Give the preparation type.
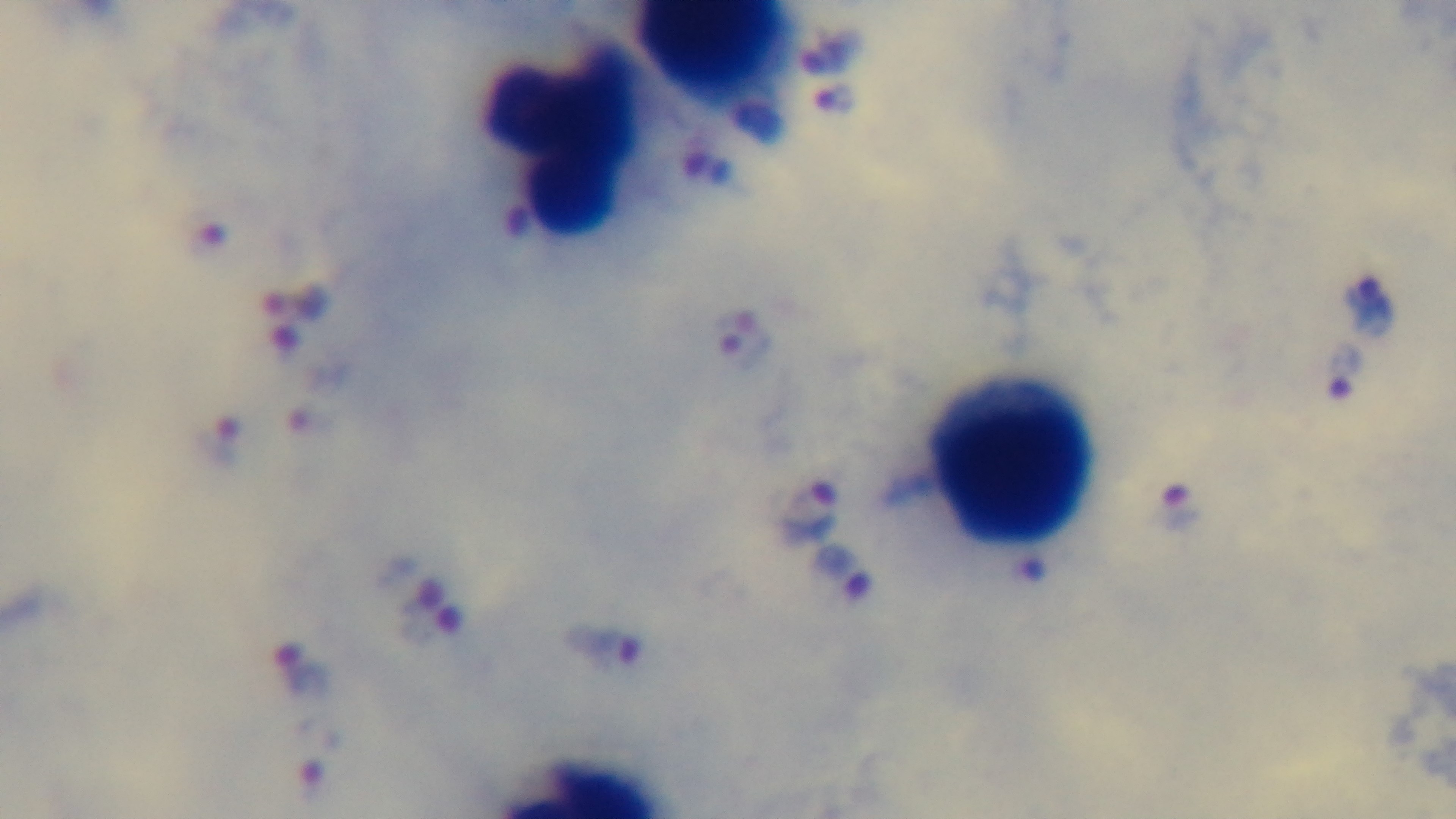
Thick.

{
  "stain": "Giemsa",
  "capture": "mounted 4K digital camera",
  "objective": "100x oil immersion",
  "malaria_status": "infected",
  "modality": "light microscopy",
  "field_of_view": "single"
}